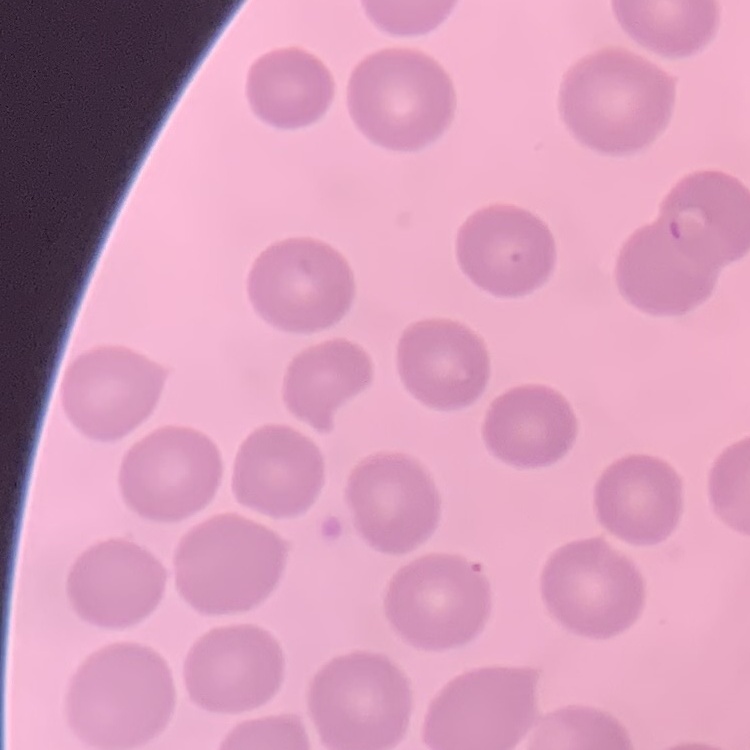

Summary:
  - Red blood cell morphology: no rouleaux formation
  - Image type: square crop of a larger photomicrograph
  - Preparation: thin blood smear
  - Stain: Field's or Giemsa